Outline each Plasmodium ovale-infected red blood cell.
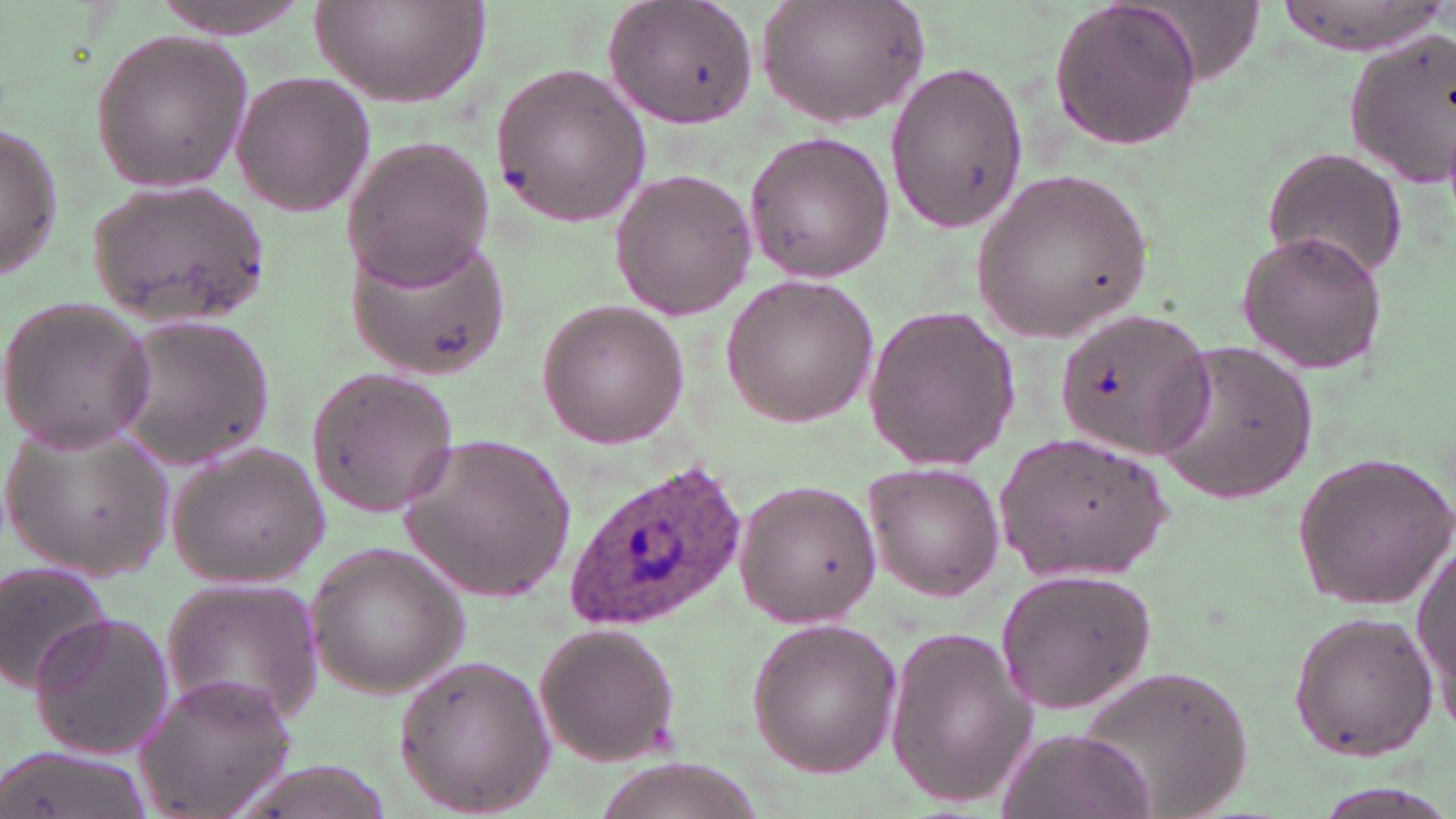

Approximate bounding boxes as [x1, y1, x2, y2] in pixels.
Plasmodium ovale-infected red blood cells: [563, 458, 749, 631].

Summary:
  - Uninfected red blood cell locations: [153, 0, 318, 39], [603, 0, 759, 130], [755, 0, 929, 128], [1045, 0, 1204, 153], [1271, 0, 1446, 56], [313, 1, 490, 108], [86, 28, 254, 194], [1344, 32, 1454, 187], [885, 61, 1028, 230], [489, 64, 653, 228], [229, 69, 375, 217], [0, 123, 63, 280], [742, 130, 895, 282], [339, 135, 494, 289], [1263, 147, 1404, 284], [608, 167, 755, 320], [973, 167, 1153, 343], [89, 182, 273, 327], [345, 228, 512, 378], [1234, 229, 1391, 376], [722, 273, 880, 427], [0, 295, 156, 452], [535, 299, 690, 448], [1051, 301, 1225, 466], [861, 302, 1023, 473], [109, 314, 277, 467], [1152, 340, 1318, 503], [304, 367, 460, 515], [4, 417, 174, 581], [993, 431, 1174, 586], [398, 432, 575, 602], [166, 442, 329, 587], [1290, 448, 1456, 609], [867, 461, 1006, 600], [728, 473, 885, 629], [1412, 532, 1454, 720], [305, 541, 468, 697], [0, 558, 112, 695], [994, 565, 1157, 715], [160, 579, 325, 731], [1286, 610, 1439, 762], [27, 611, 175, 761], [743, 617, 902, 779], [534, 621, 682, 767], [883, 622, 1036, 811], [390, 650, 558, 815], [1075, 664, 1256, 819], [135, 670, 299, 819], [995, 726, 1154, 819], [1, 741, 150, 819]
  - Slide-level diagnosis: Plasmodium ovale
  - Stain: May-Grünwald-Giemsa
  - Magnification: 1000x
  - Modality: optical microscopy
  - Preparation: thin blood smear
  - Field of view: one of a larger specimen
  - Image size: 1456×819 pixels